Identify the parasite.
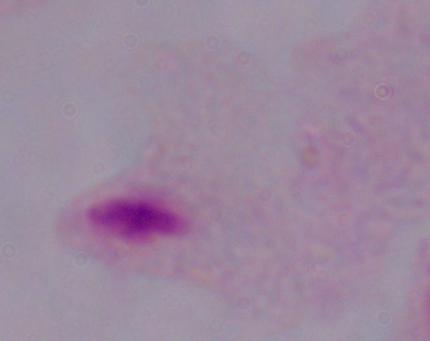

This is a trichomonad.

Summary:
  - Magnification: 1000x
  - Modality: micrograph